Give the position of every Plasmodium parasite.
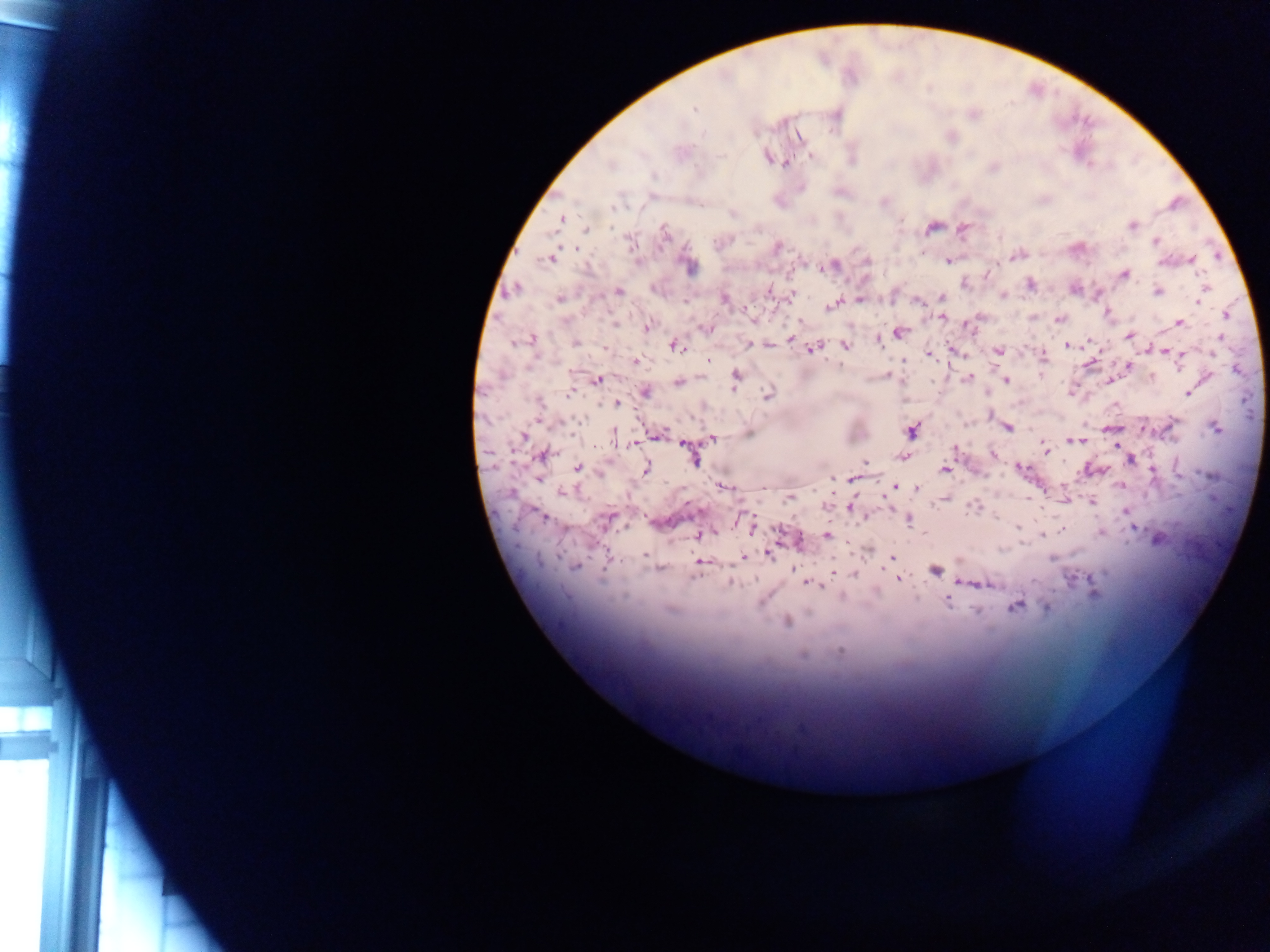

Approximate centers as (x, y) in pixels.
Plasmodium parasites: (695, 108), (950, 136), (799, 138), (767, 156), (810, 156), (786, 162), (993, 167), (800, 187), (883, 201), (733, 214), (560, 219), (1132, 225), (933, 227), (963, 228), (587, 229), (664, 232), (1155, 241), (777, 247), (1077, 248), (1017, 255), (550, 257), (865, 260), (948, 260), (1191, 260), (689, 265), (827, 266), (988, 274), (1123, 274), (964, 282), (1029, 284), (515, 288), (656, 288), (1074, 289), (1203, 290), (618, 291), (768, 291), (1158, 291), (792, 294), (1003, 294), (723, 297), (940, 297), (558, 298), (860, 299), (1198, 299), (919, 300), (835, 303), (745, 310), (1107, 313), (1226, 315), (942, 317), (1059, 319), (1179, 322), (646, 327), (704, 327), (898, 331), (1130, 336), (790, 338), (1219, 338), (530, 339), (878, 339), (523, 340), (1089, 341), (573, 342), (749, 343), (767, 344), (1066, 344), (673, 345), (845, 345), (607, 348), (811, 348), (951, 348), (998, 350), (1165, 351), (928, 354), (1181, 354), (1041, 356), (636, 360), (709, 360), (1088, 363), (839, 364), (1129, 365), (1237, 369), (886, 375), (969, 377), (1152, 377), (1207, 377), (734, 378), (595, 379), (1006, 379), (679, 381), (1107, 381), (572, 392), (645, 392), (1187, 393), (768, 395), (617, 402), (1007, 427), (1107, 428), (1215, 428), (910, 430), (747, 432), (658, 434), (522, 436), (614, 437), (712, 438), (1080, 439), (1073, 440), (632, 443), (1116, 445), (955, 448), (1046, 449), (992, 454), (542, 455), (691, 455), (904, 455), (1130, 460), (865, 462), (1019, 467), (578, 468), (645, 468), (1090, 469), (945, 470), (538, 477), (831, 477), (854, 478), (1120, 485), (723, 486), (894, 486), (764, 487), (917, 488), (565, 491), (790, 497), (943, 498), (1064, 498), (1091, 501), (829, 503), (851, 506), (976, 506), (1125, 510), (542, 515), (606, 519), (907, 519), (1132, 526), (752, 527), (1017, 527), (1062, 529), (1100, 532), (698, 534), (827, 534), (1042, 535), (1158, 538), (798, 540), (865, 549), (768, 553), (645, 554), (743, 557), (891, 558), (700, 561), (575, 565), (660, 568), (793, 568), (831, 569), (935, 570), (854, 575), (898, 578), (731, 582), (966, 582), (984, 583), (809, 584), (1092, 590), (947, 600), (1015, 605), (1047, 607), (786, 620), (803, 655).

Summary:
  - Capture: mobile-phone photograph through a microscope
  - Country: Ghana
  - Field of view: single
  - Preparation: thick blood film
  - Image size: 1270×952 pixels